Identify the parasite.
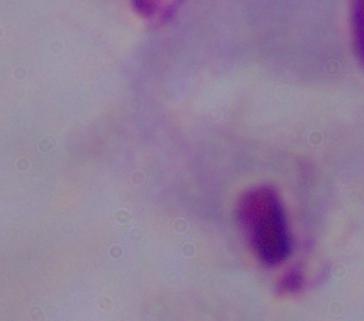

This is a trichomonad.

1000x magnification. Micrograph.